Report the malaria status of this cell.
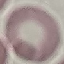

Uninfected.

Thin blood film. Cell patch, automatically extracted from a larger field of view and resized to 64 × 64 pixels. Giemsa stain. Photographed with a smartphone camera at the microscope eyepiece.